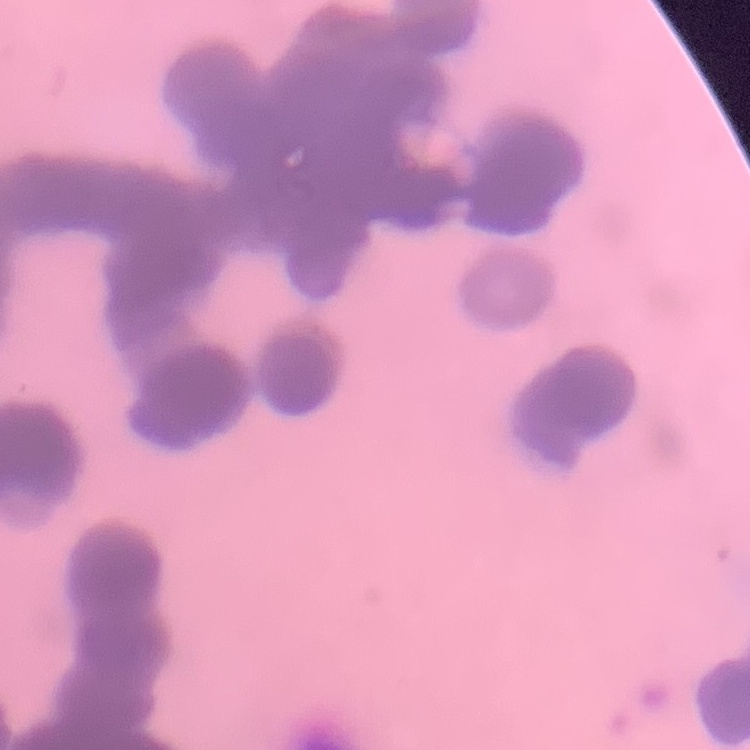

The red blood cells show rouleaux formation. Thin peripheral smear. Field's or Giemsa stain. Square crop of a larger photomicrograph.